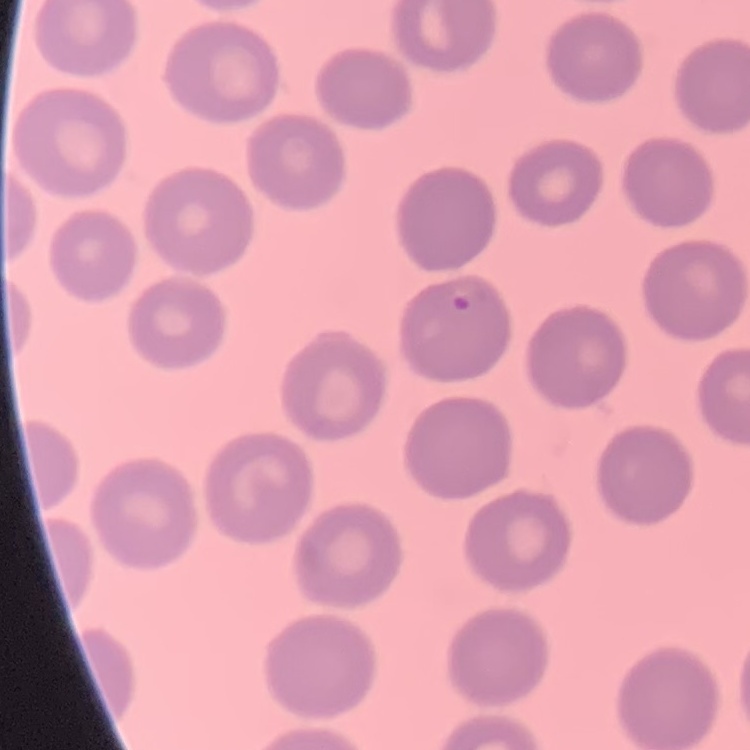 The red blood cells exhibit no rouleaux formation. Stained with either Field's or Giemsa. Square crop of a larger photomicrograph. Thin blood film.